Classify this cell by malaria status.
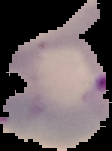
It is parasitized.

The area outside the segmented cell region is set to black. Image is 112×151 pixels. From a thin blood film.